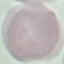
Result: no malaria parasites detected. Photographed with a smartphone camera at the microscope eyepiece. Cell patch, automatically extracted from a larger field of view and resized to 64 × 64 pixels. Thin blood smear. Giemsa-stained preparation.